Identify the parasite.
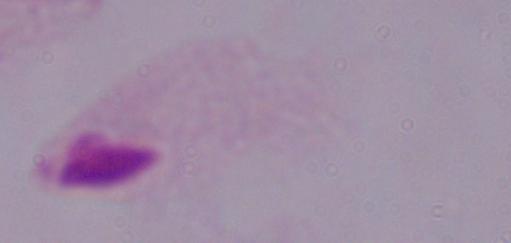

This is a trichomonad.

Summary:
  - Magnification: 1000x
  - Modality: micrograph